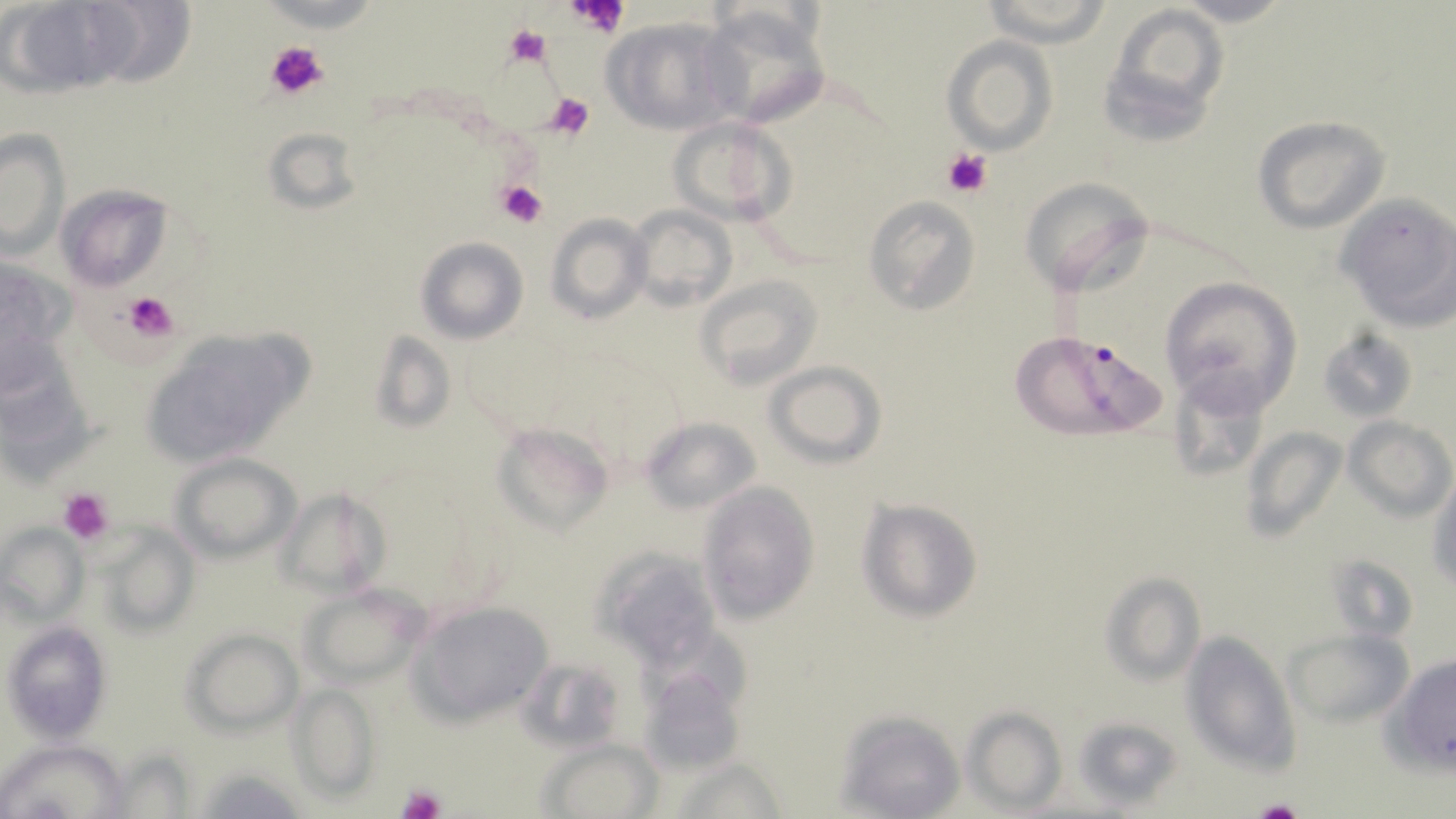
slide-level diagnosis = Plasmodium falciparum
stain = May-Grünwald-Giemsa
Plasmodium falciparum-infected red blood cell locations = approximate bounding boxes as (x1,y1)-(x2,y2) corner pairs in pixels: (1008,329)-(1173,443)
magnification = 1000x
modality = light microscopy
image size = 1456×819 pixels
preparation = thin blood film
field of view = one of a larger specimen
uninfected red blood cell locations = approximate bounding boxes as (x1,y1)-(x2,y2) corner pairs in pixels: (979,0)-(1114,46), (1171,0)-(1297,28), (2,2)-(118,96), (1097,2)-(1232,145), (695,4)-(834,129), (601,17)-(732,133), (942,36)-(1058,154), (1252,115)-(1392,235), (667,117)-(794,224), (264,125)-(361,214), (0,130)-(69,258), (1019,176)-(1155,295), (55,183)-(174,291), (1336,194)-(1456,329), (864,195)-(981,315), (626,204)-(737,312), (546,213)-(650,324), (416,237)-(528,344), (0,256)-(76,375), (693,273)-(823,391), (1160,276)-(1303,413), (137,327)-(307,468), (1319,328)-(1417,424), (370,332)-(456,435), (0,347)-(96,481), (766,361)-(887,467), (1166,366)-(1280,488), (1346,416)-(1455,520), (641,417)-(762,513), (493,421)-(614,534), (1243,425)-(1347,543), (174,454)-(298,561), (1428,472)-(1456,595), (697,482)-(820,621), (274,487)-(389,601), (857,499)-(982,623), (96,525)-(200,638), (0,526)-(87,622), (589,543)-(724,670), (1100,572)-(1206,688), (298,582)-(429,686), (409,600)-(555,727), (5,622)-(110,741), (182,628)-(302,734), (1285,628)-(1413,727), (1180,630)-(1301,774), (515,655)-(629,753), (1389,655)-(1456,770), (637,664)-(746,776), (290,686)-(378,799), (961,707)-(1067,813), (832,710)-(964,819), (1070,717)-(1182,809), (540,738)-(662,818), (0,740)-(128,817), (106,751)-(197,815), (672,756)-(793,817), (196,768)-(308,817)
platelet locations = approximate bounding boxes as (x1,y1)-(x2,y2) corner pairs in pixels: (567,0)-(630,39), (505,22)-(552,70), (264,39)-(328,102), (546,93)-(593,137), (944,147)-(994,197), (497,180)-(548,229), (124,292)-(177,340), (57,485)-(116,545), (395,783)-(447,819), (1246,797)-(1308,819)